Locate and identify every blood parasite.
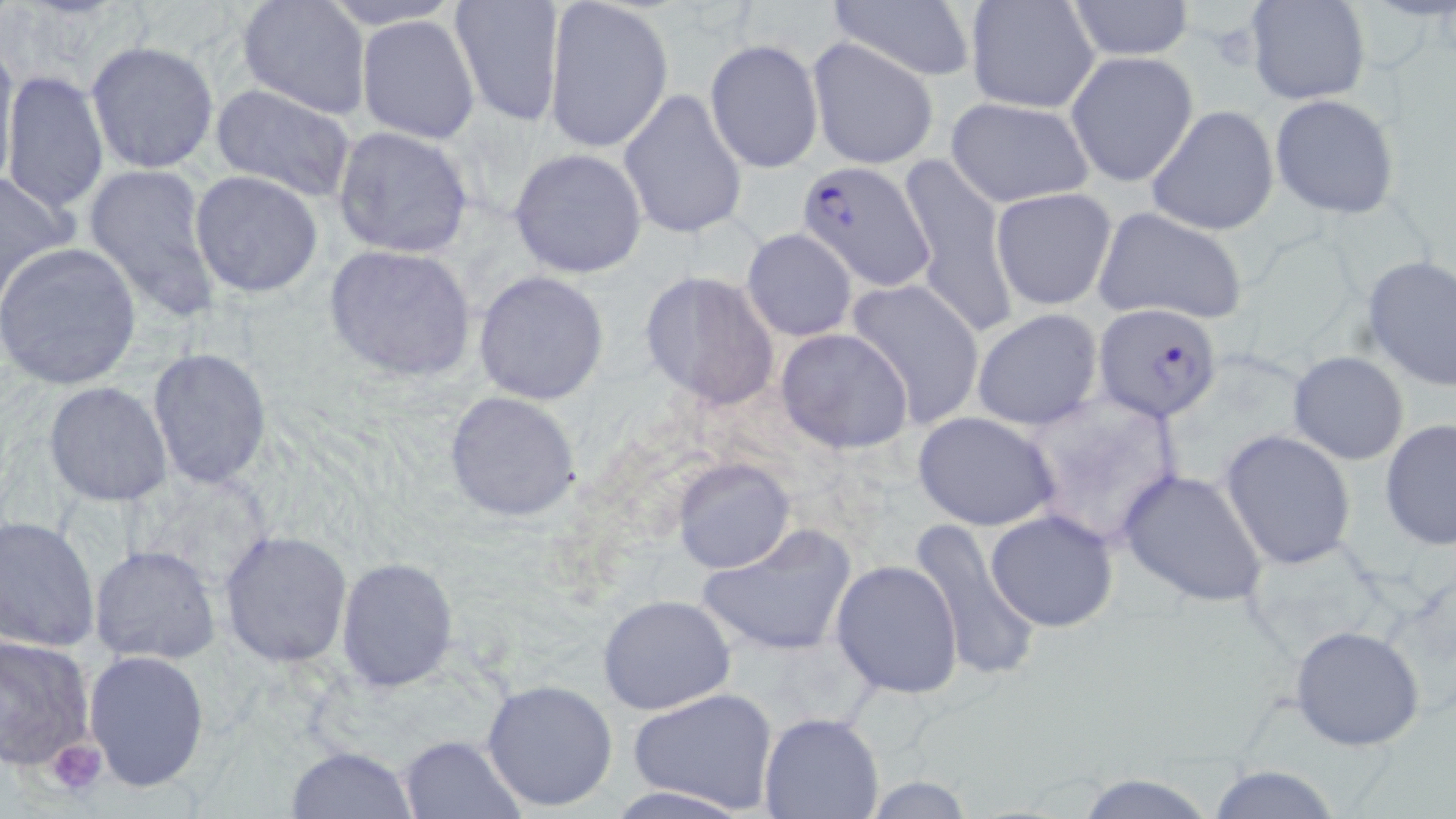
Approximate bounding boxes as [x1, y1, x2, y2] in pixels.
Plasmodium falciparum-infected red blood cells: [798, 160, 935, 291], [1094, 302, 1225, 422].
No Plasmodium ovale, Plasmodium malariae, Plasmodium vivax, Babesia divergens, or Trypanosoma brucei observed.

Summary:
  - Uninfected red blood cell locations: [237, 0, 372, 119], [315, 0, 465, 29], [448, 0, 566, 127], [542, 0, 674, 155], [821, 0, 980, 83], [1246, 0, 1369, 105], [964, 1, 1101, 115], [1066, 1, 1195, 60], [355, 15, 481, 145], [807, 37, 941, 170], [705, 38, 823, 174], [86, 40, 221, 175], [0, 45, 19, 195], [1068, 49, 1199, 187], [1, 69, 109, 217], [208, 84, 359, 203], [618, 88, 748, 241], [1270, 93, 1400, 219], [946, 95, 1096, 208], [1145, 104, 1279, 237], [330, 126, 476, 259], [508, 148, 647, 279], [899, 156, 1016, 336], [81, 161, 222, 317], [0, 167, 80, 292], [190, 170, 325, 298], [990, 188, 1118, 312], [1092, 204, 1250, 325], [742, 229, 859, 342], [0, 242, 143, 390], [323, 243, 478, 381], [1359, 255, 1456, 393], [472, 270, 610, 406], [639, 271, 779, 410], [843, 278, 987, 427], [971, 309, 1105, 431], [774, 329, 913, 454], [148, 348, 271, 487], [1288, 350, 1409, 464], [44, 380, 172, 506], [442, 390, 585, 524], [912, 411, 1061, 531], [1379, 421, 1456, 555], [1220, 430, 1356, 569], [673, 458, 794, 573], [1117, 468, 1270, 607], [985, 509, 1118, 632], [1, 515, 101, 652], [907, 520, 1043, 682], [695, 525, 857, 660], [218, 530, 352, 667], [1237, 536, 1397, 663], [90, 545, 221, 664], [335, 556, 459, 694], [831, 559, 964, 699], [597, 595, 736, 716], [1288, 625, 1426, 750], [0, 633, 96, 771], [82, 648, 211, 793], [481, 677, 621, 813], [627, 687, 780, 814], [759, 712, 885, 819], [396, 734, 525, 818], [284, 745, 418, 818], [1205, 765, 1344, 819], [1073, 770, 1220, 819], [858, 777, 980, 816]
  - Platelet locations: [1200, 18, 1262, 72], [46, 738, 106, 797]
  - Slide-level diagnosis: Plasmodium falciparum
  - Preparation: thin blood film
  - Image size: 1456×819 pixels
  - Stain: May-Grünwald-Giemsa
  - Modality: light microscopy
  - Field of view: one of a larger specimen
  - Magnification: 1000x